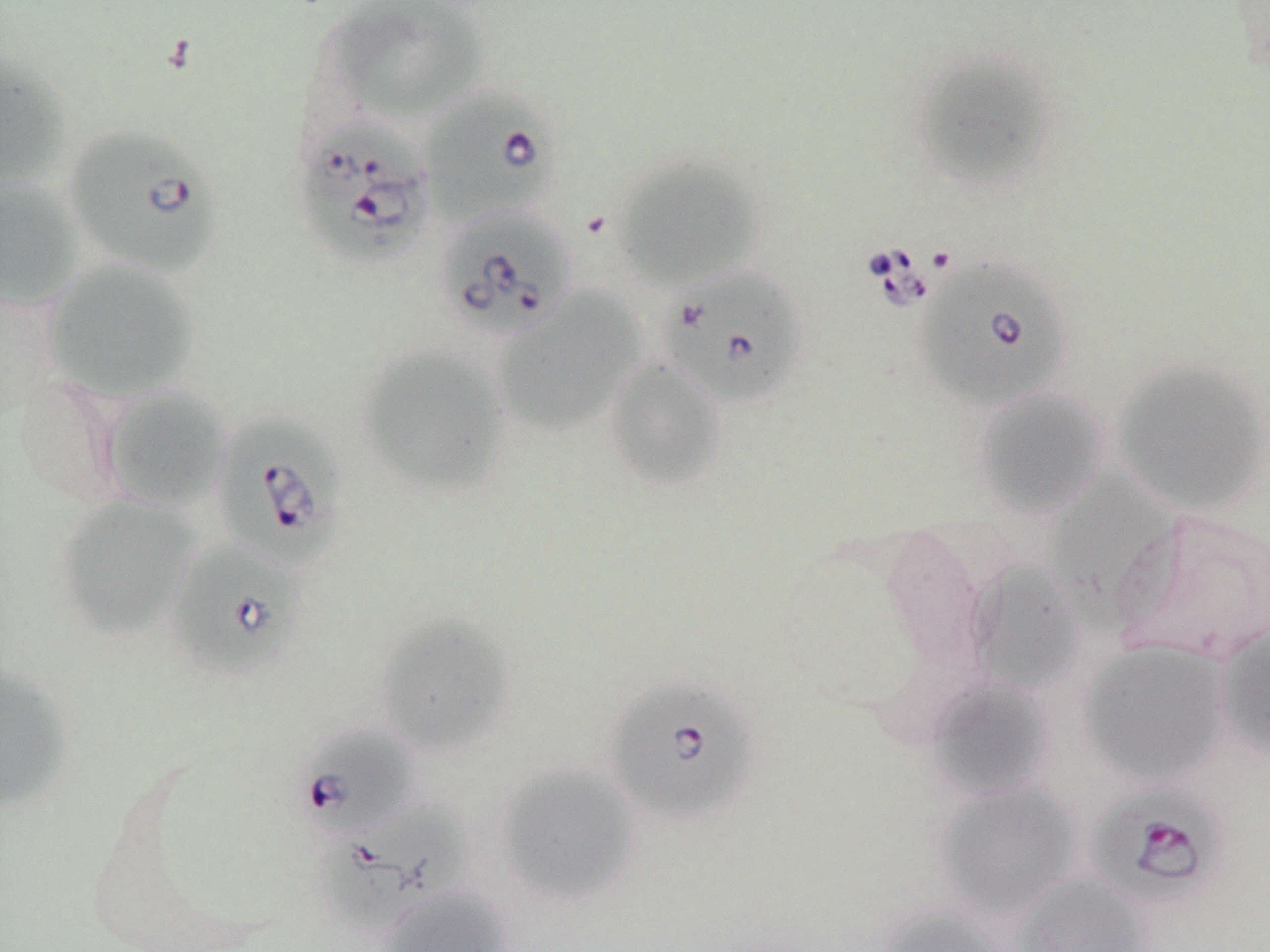

Summary:
  - Coordinate format: approximate bounding boxes as named x1/y1/x2/y2 corners in pixels
  - Babesia divergens-infected red blood cell locations: (x1=419, y1=85, x2=561, y2=229), (x1=290, y1=117, x2=437, y2=268), (x1=62, y1=124, x2=226, y2=279), (x1=434, y1=206, x2=577, y2=342), (x1=911, y1=257, x2=1074, y2=412), (x1=657, y1=267, x2=809, y2=411), (x1=211, y1=408, x2=349, y2=570), (x1=164, y1=538, x2=305, y2=680), (x1=602, y1=673, x2=761, y2=827), (x1=293, y1=725, x2=418, y2=841), (x1=1084, y1=781, x2=1230, y2=908), (x1=321, y1=795, x2=473, y2=924)
  - Uninfected red blood cell locations: (x1=322, y1=1, x2=488, y2=124), (x1=909, y1=50, x2=1054, y2=190), (x1=0, y1=51, x2=72, y2=196), (x1=612, y1=154, x2=764, y2=289), (x1=0, y1=176, x2=86, y2=313), (x1=40, y1=258, x2=202, y2=402), (x1=492, y1=289, x2=643, y2=436), (x1=356, y1=345, x2=511, y2=498), (x1=603, y1=357, x2=728, y2=491), (x1=1112, y1=359, x2=1270, y2=516), (x1=11, y1=374, x2=126, y2=506), (x1=99, y1=385, x2=232, y2=512), (x1=972, y1=388, x2=1108, y2=520), (x1=1043, y1=468, x2=1177, y2=625), (x1=54, y1=495, x2=201, y2=640), (x1=1111, y1=507, x2=1270, y2=666), (x1=967, y1=560, x2=1083, y2=695), (x1=374, y1=615, x2=515, y2=757), (x1=1215, y1=624, x2=1270, y2=761), (x1=1078, y1=640, x2=1230, y2=788), (x1=0, y1=662, x2=75, y2=814), (x1=926, y1=678, x2=1056, y2=801), (x1=494, y1=763, x2=640, y2=906), (x1=935, y1=779, x2=1082, y2=919), (x1=1012, y1=873, x2=1155, y2=952), (x1=377, y1=885, x2=514, y2=952), (x1=875, y1=905, x2=1010, y2=952)
  - Slide-level diagnosis: Babesia divergens
  - Image size: 1270×952 pixels
  - Field of view: one of a larger specimen
  - Magnification: 1000x
  - Stain: May-Grünwald-Giemsa
  - Preparation: thin blood smear
  - Modality: optical microscopy